Describe the morphology of the erythrocytes.
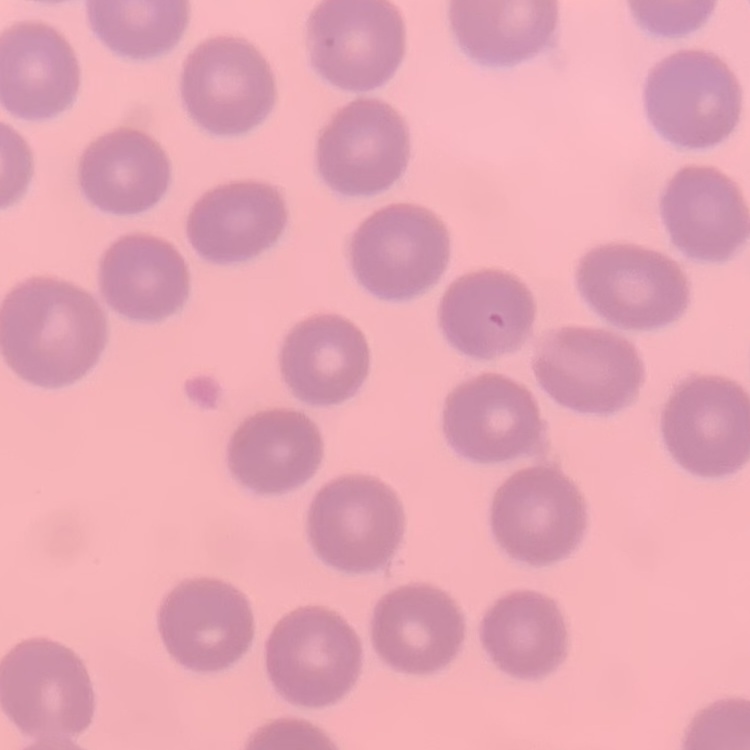

They show no rouleaux formation.

Thin blood smear. Square crop of a larger photomicrograph. Stained with either Field's or Giemsa.